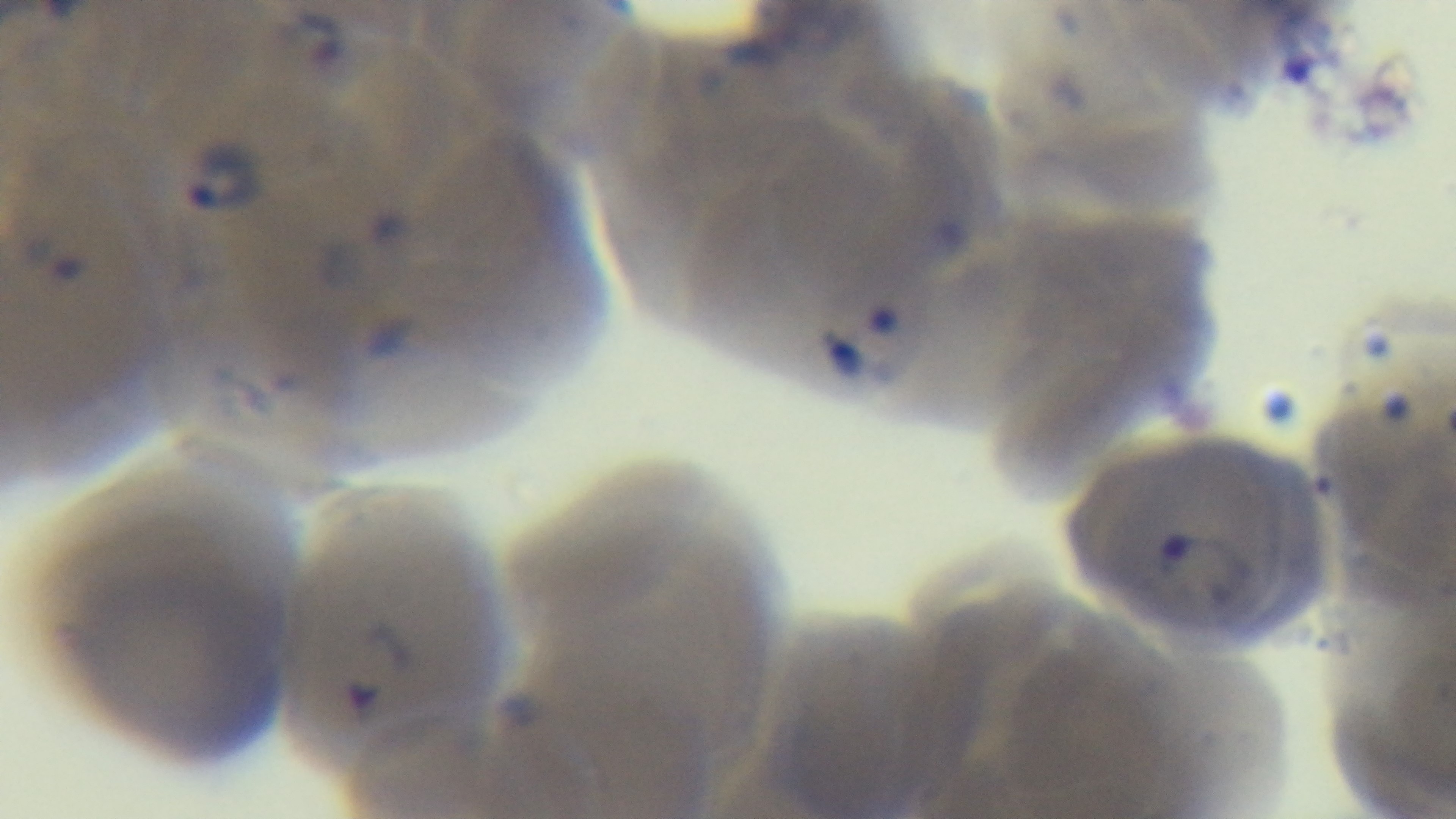
100x oil-immersion objective. Captured with a mounted 4K digital camera. Preparation: thin smear. Giemsa stain. Single field of view. Malaria status: infected. Light microscopy.